Outline each uninfected red blood cell.
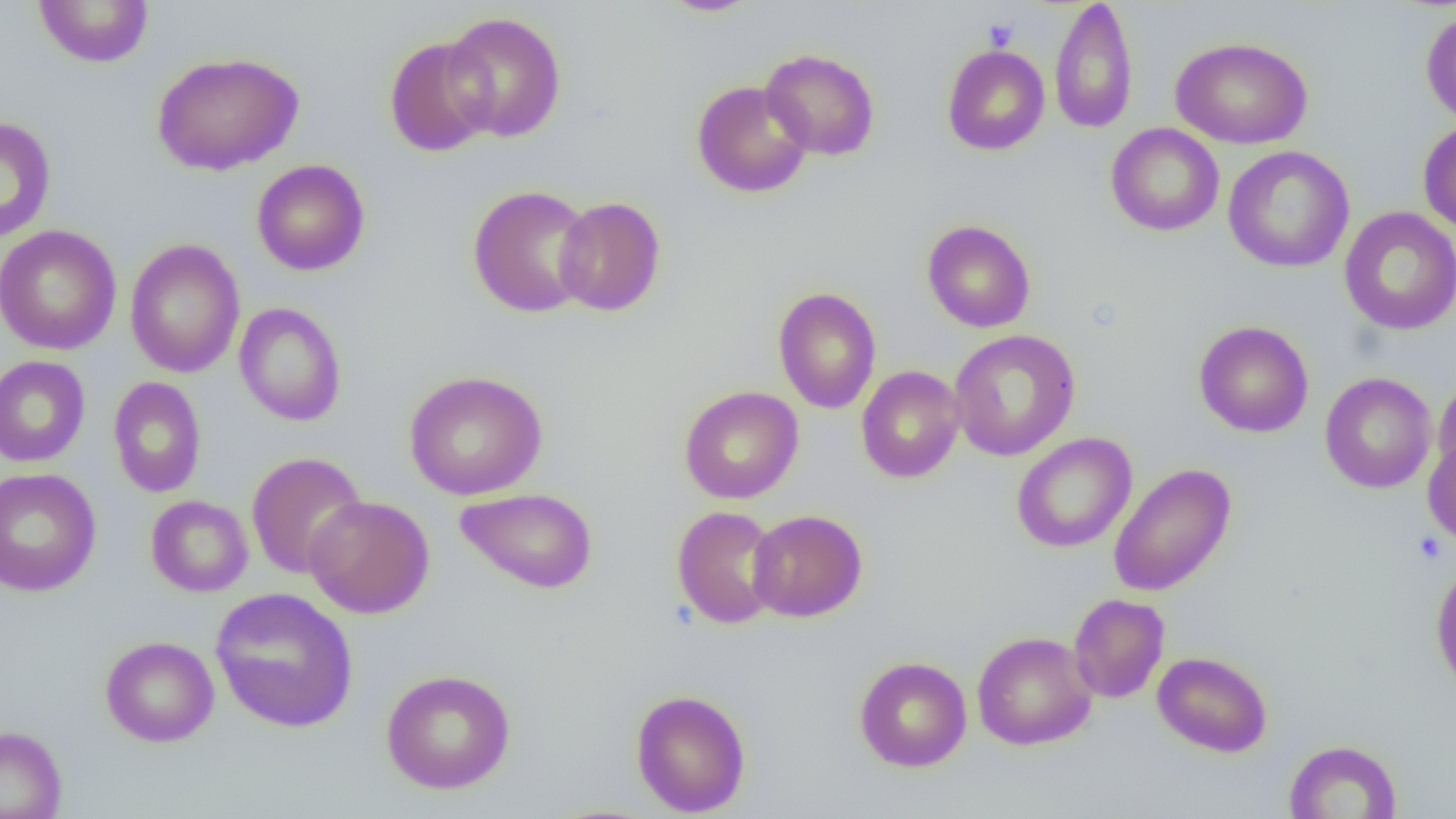
Approximate bounding boxes as [x1, y1, x2, y2] in pixels.
Uninfected red blood cells: [657, 0, 764, 17], [1049, 0, 1138, 135], [33, 1, 154, 68], [1420, 8, 1456, 127], [443, 11, 566, 142], [384, 36, 496, 157], [1172, 36, 1312, 149], [942, 44, 1050, 156], [760, 48, 880, 161], [152, 52, 304, 175], [692, 80, 813, 198], [0, 116, 56, 244], [1418, 120, 1456, 235], [1105, 122, 1224, 237], [1223, 145, 1355, 273], [252, 159, 370, 276], [467, 184, 596, 318], [553, 196, 666, 316], [1339, 206, 1456, 335], [922, 219, 1036, 333], [0, 225, 122, 356], [124, 238, 246, 378], [773, 286, 881, 414], [233, 302, 347, 426], [1193, 320, 1313, 437], [949, 329, 1081, 461], [0, 355, 91, 467], [856, 365, 965, 483], [404, 369, 547, 500], [1319, 372, 1436, 494], [1433, 373, 1456, 483], [108, 377, 207, 498], [679, 386, 803, 504], [1011, 432, 1137, 553], [1423, 435, 1456, 546], [246, 452, 367, 579], [1108, 463, 1236, 597], [0, 467, 102, 597], [455, 487, 598, 594], [146, 495, 253, 597], [304, 495, 435, 618], [671, 505, 783, 629], [747, 509, 868, 622], [1430, 562, 1456, 694], [210, 588, 359, 733], [1069, 593, 1169, 703], [972, 631, 1098, 751], [100, 635, 219, 747], [1152, 650, 1273, 757], [854, 656, 972, 772], [380, 668, 516, 794], [630, 689, 751, 816], [0, 725, 67, 819], [1283, 740, 1402, 819].

Platelet locations: [982, 18, 1019, 51], [1413, 532, 1447, 565]. Slide-level diagnosis: no evidence of blood parasites. One field of a larger specimen. Image is 1456×819 pixels. Thin blood film. Optical microscopy. Captured at 1000x magnification.